Identify the cell.
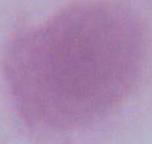

This is an erythrocyte.

Micrograph. Captured at 1000x magnification.